Outline each Plasmodium falciparum-infected red blood cell.
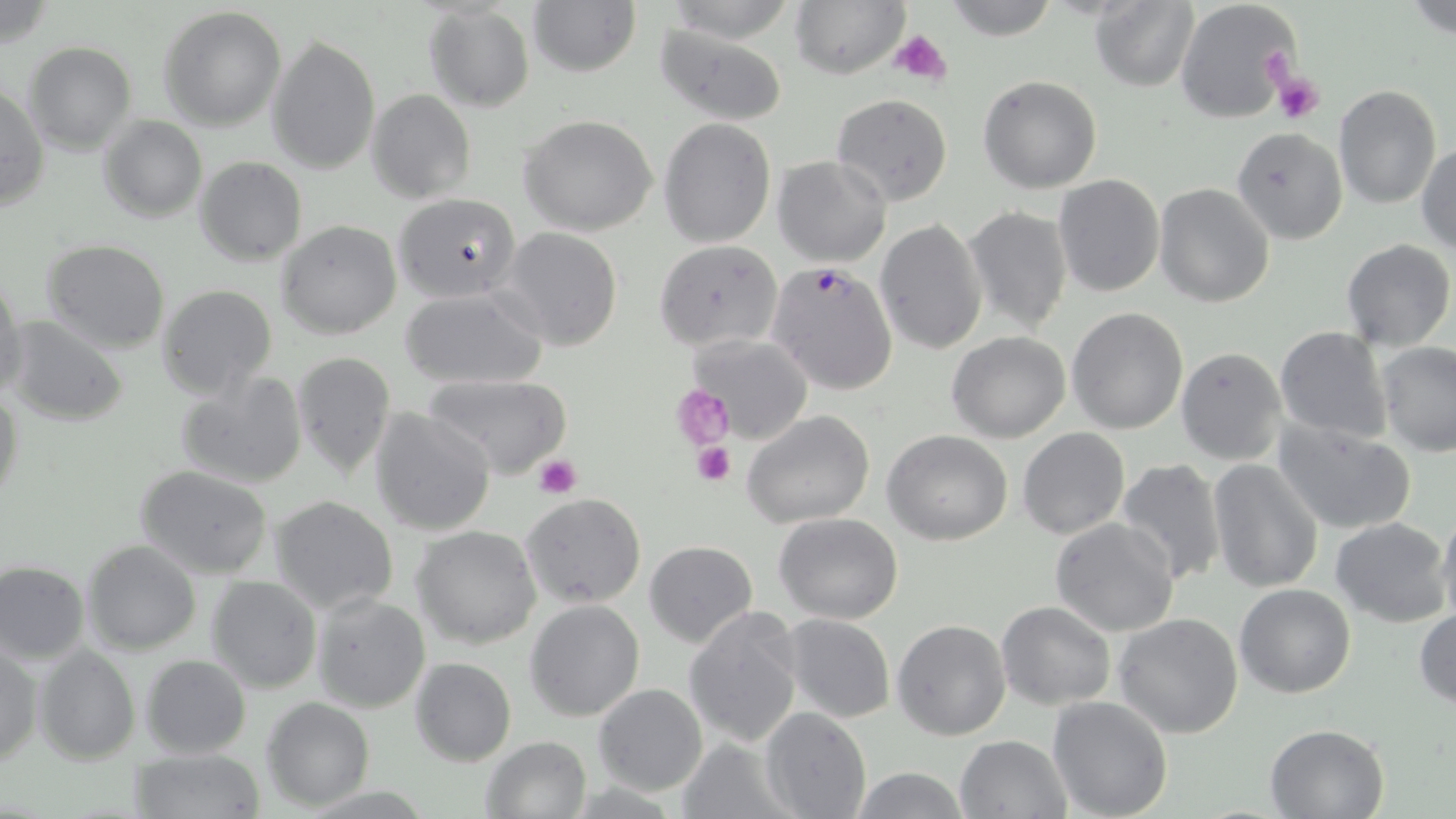

Approximate bounding boxes as [x1, y1, x2, y2] in pixels.
Plasmodium falciparum-infected red blood cells: [766, 262, 898, 395].

Uninfected red blood cell locations: [528, 0, 641, 76], [663, 0, 800, 44], [942, 0, 1059, 42], [1174, 0, 1300, 124], [791, 1, 908, 77], [1090, 1, 1198, 90], [1403, 2, 1456, 39], [424, 4, 535, 114], [160, 7, 287, 130], [653, 24, 790, 124], [266, 34, 381, 175], [23, 41, 136, 155], [978, 74, 1103, 194], [1334, 83, 1442, 210], [0, 85, 49, 210], [368, 89, 476, 203], [830, 93, 952, 207], [98, 114, 207, 223], [519, 114, 660, 237], [658, 118, 775, 247], [1231, 127, 1347, 245], [1416, 143, 1456, 255], [772, 156, 892, 267], [194, 157, 306, 266], [1052, 174, 1165, 297], [1154, 183, 1274, 307], [395, 193, 521, 302], [962, 205, 1071, 335], [875, 219, 989, 357], [276, 220, 403, 338], [498, 227, 625, 351], [653, 239, 782, 351], [1341, 239, 1454, 350], [41, 240, 170, 353], [0, 275, 26, 402], [156, 284, 277, 401], [400, 286, 548, 389], [1066, 307, 1190, 434], [5, 316, 129, 426], [1275, 326, 1392, 444], [947, 330, 1071, 442], [689, 335, 812, 442], [1374, 341, 1456, 457], [1175, 346, 1287, 465], [291, 352, 396, 477], [175, 370, 309, 490], [423, 373, 571, 479], [0, 383, 25, 511], [370, 407, 496, 537], [742, 410, 875, 529], [1274, 415, 1418, 537], [1017, 427, 1130, 539], [883, 429, 1013, 545], [1116, 458, 1228, 587], [1208, 459, 1324, 593], [135, 464, 273, 578], [521, 493, 646, 609], [269, 494, 400, 616], [1436, 506, 1456, 630], [774, 512, 903, 624], [1331, 516, 1452, 626], [1049, 518, 1180, 638], [412, 526, 542, 649], [82, 540, 201, 654], [644, 541, 758, 647], [0, 563, 89, 661], [207, 575, 322, 693], [1234, 583, 1358, 698], [313, 593, 430, 713], [524, 599, 646, 721], [996, 601, 1116, 711], [682, 607, 805, 748], [1413, 608, 1456, 708], [1114, 611, 1243, 739], [779, 614, 896, 725], [891, 618, 1012, 740], [1, 642, 42, 766], [33, 645, 140, 764], [141, 654, 251, 758], [409, 657, 516, 764], [594, 684, 708, 797], [1047, 695, 1173, 819], [262, 697, 375, 811], [759, 707, 871, 819], [1263, 723, 1390, 818], [481, 736, 592, 818], [954, 736, 1072, 819], [679, 737, 795, 819], [131, 748, 265, 819], [849, 767, 972, 819]. Platelet locations: [890, 29, 953, 84], [1273, 70, 1324, 123], [673, 385, 735, 450], [692, 439, 733, 486], [532, 453, 581, 499]. Slide-level diagnosis: Plasmodium falciparum. Single field of view. Optical microscopy. Image is 1456×819 pixels. Thin blood film. May-Grünwald-Giemsa stain. 1000x magnification.